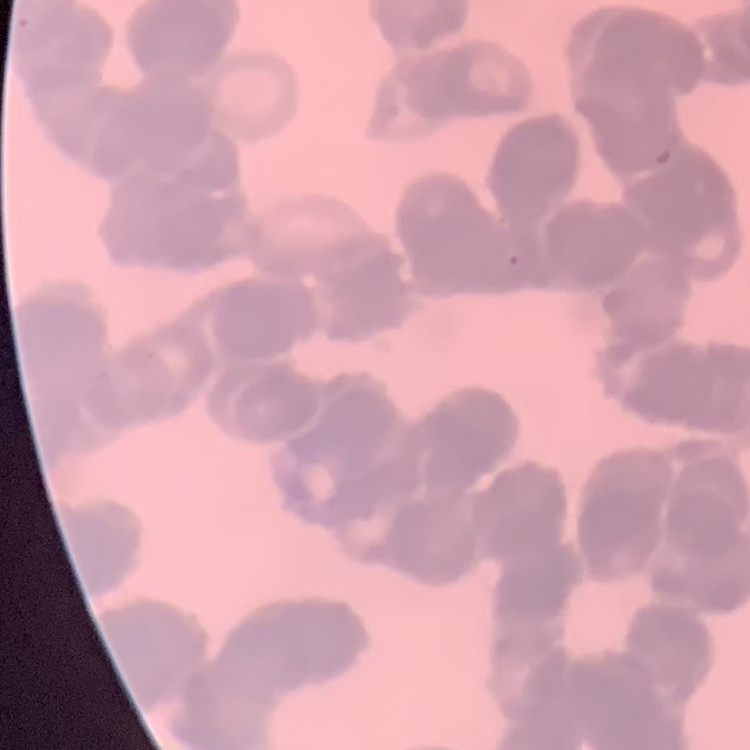 The red blood cells show rouleaux formation. One tile cut from a larger photomicrograph. Thin peripheral smear. Field's or Giemsa stain.